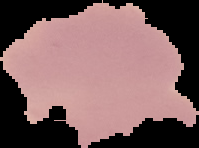 Result: no malaria parasites detected. Image is 199×148 pixels. From a thin blood smear. Segmented cell region on a black background.